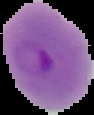
The area outside the segmented cell region is set to black. From a thin blood film. Result: Plasmodium parasites identified. Image is 94×115 pixels.